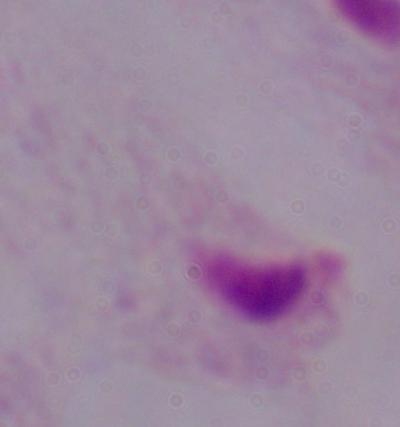
Summary:
  - Identification: trichomonad
  - Modality: micrograph
  - Magnification: 1000x